Point out every malaria parasite.
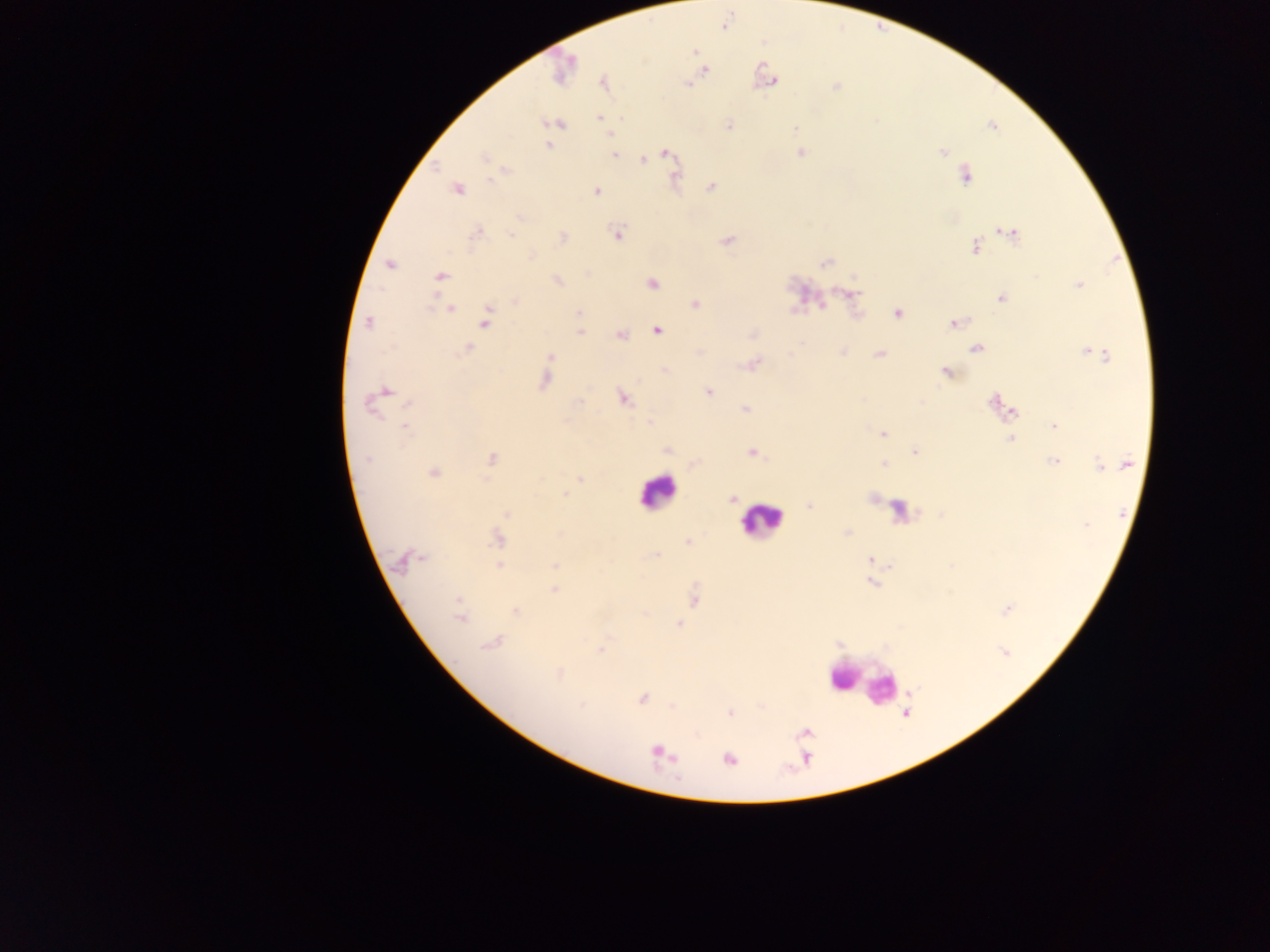
Approximate centers as (x, y) in pixels.
Malaria parasites: (694, 51), (564, 68), (703, 69), (774, 81), (687, 82), (604, 83), (835, 86), (599, 118), (555, 124), (729, 125), (795, 126), (610, 133), (549, 146), (800, 152), (943, 152), (613, 153), (664, 154), (486, 159), (643, 160), (502, 171), (965, 174), (675, 176), (710, 187), (456, 189), (596, 191), (476, 233), (616, 233), (1010, 233), (562, 238), (727, 240), (976, 246), (824, 262), (389, 264), (440, 275), (556, 280), (651, 282), (1078, 284), (850, 293), (1002, 298), (515, 300), (695, 304), (821, 305), (449, 308), (578, 313), (897, 313), (485, 318), (369, 322), (954, 323), (657, 330), (580, 332), (753, 333), (620, 335), (468, 348), (976, 348), (843, 352), (1090, 352), (880, 353), (549, 356), (752, 364), (664, 371), (947, 372), (544, 378), (708, 392), (379, 395), (623, 398), (995, 402), (1002, 406), (745, 408), (1012, 411), (1054, 425), (404, 426), (883, 433), (1010, 438), (668, 450), (752, 452), (915, 452), (491, 459), (1054, 461), (695, 464), (1125, 464), (885, 465), (1100, 465), (432, 472), (580, 478), (566, 495), (872, 497), (731, 499), (809, 506), (506, 513), (846, 533), (498, 538), (688, 542), (654, 555), (407, 559), (868, 560), (499, 565), (554, 565), (871, 582), (554, 590), (693, 597), (1006, 609), (515, 611), (460, 612), (678, 624), (490, 643), (600, 649), (1004, 653), (559, 674), (642, 698), (730, 712), (805, 732), (656, 752), (728, 758).

Leukocyte locations: (657, 491), (900, 511), (761, 518), (849, 676), (869, 684), (884, 689). Single field of view. Image is 1270×952 pixels. Thick blood film. Mobile-phone photograph taken through the microscope. Sample from Ghana.